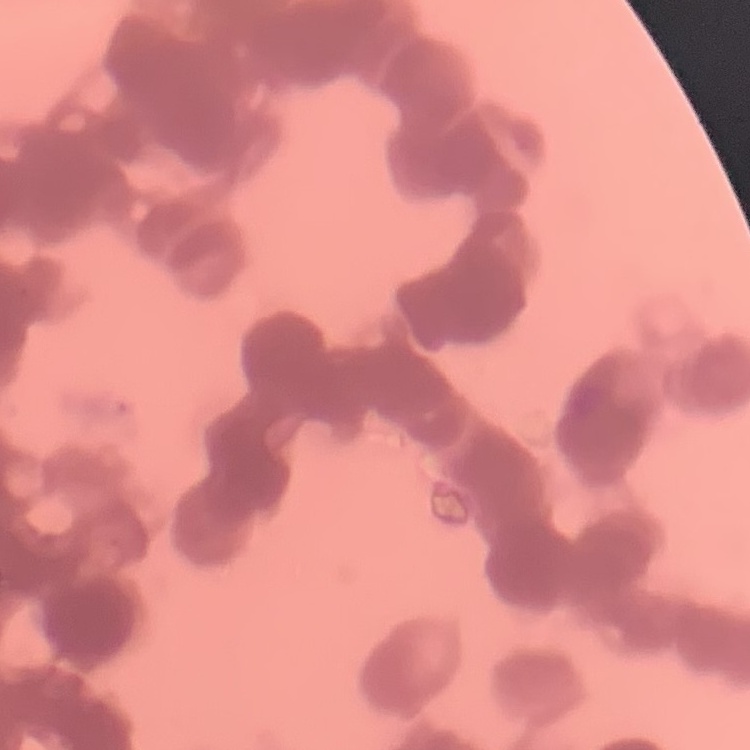 The red blood cells exhibit rouleaux formation. Thin blood film. Square crop of a larger photomicrograph. Field's or Giemsa stain.